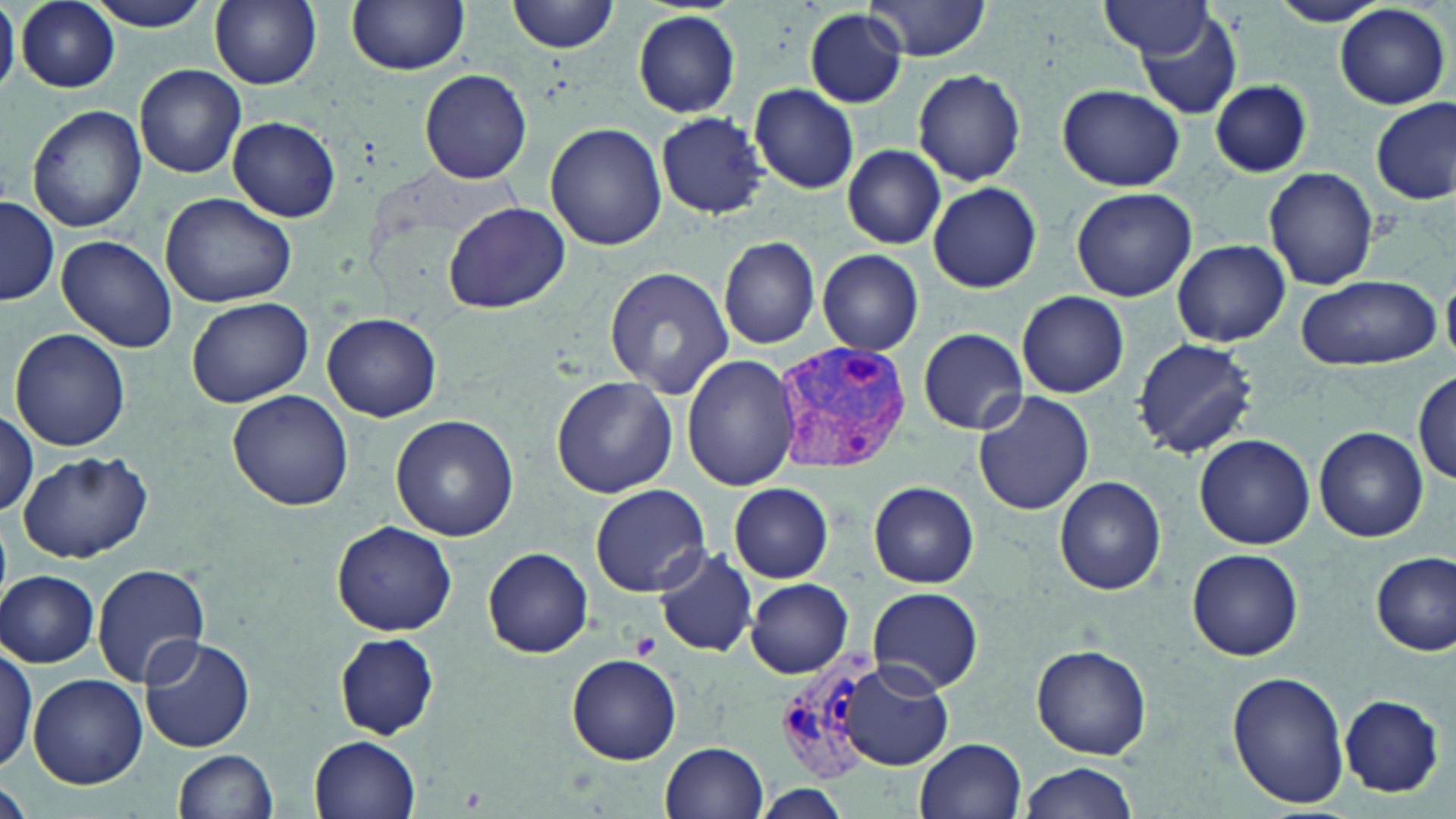

slide-level diagnosis = Plasmodium vivax
uninfected red blood cell locations = approximate bounding boxes as (x1, y1, x2, y2) in pixels: (86, 0, 217, 31), (208, 0, 322, 90), (508, 0, 619, 53), (862, 0, 993, 60), (1266, 0, 1389, 26), (346, 1, 470, 75), (15, 2, 120, 91), (1098, 2, 1213, 61), (0, 3, 19, 97), (1335, 5, 1449, 108), (805, 9, 906, 107), (1137, 9, 1242, 121), (632, 11, 740, 118), (135, 64, 246, 179), (417, 68, 533, 185), (913, 69, 1026, 185), (1209, 79, 1312, 177), (750, 84, 860, 195), (1057, 84, 1185, 191), (1372, 98, 1454, 205), (26, 104, 147, 232), (656, 110, 769, 219), (228, 117, 340, 221), (546, 122, 667, 249), (843, 145, 945, 249), (1263, 166, 1378, 291), (927, 182, 1042, 294), (1070, 187, 1198, 302), (160, 193, 300, 310), (1, 197, 60, 306), (443, 201, 570, 312), (56, 235, 178, 353), (718, 235, 822, 350), (1173, 239, 1290, 346), (817, 251, 925, 355), (605, 266, 732, 398), (1296, 273, 1442, 372), (1016, 291, 1129, 398), (187, 296, 314, 407), (323, 315, 442, 421), (9, 327, 131, 450), (918, 328, 1028, 436), (1132, 337, 1259, 460), (681, 354, 802, 490), (1413, 370, 1455, 487), (551, 375, 677, 498), (972, 389, 1093, 515), (227, 390, 354, 511), (0, 410, 39, 518), (390, 414, 519, 541), (1315, 427, 1427, 541), (1193, 433, 1316, 549), (17, 450, 152, 564), (1054, 476, 1167, 595), (868, 480, 979, 586), (728, 482, 833, 583), (590, 484, 709, 596), (332, 520, 458, 637), (483, 547, 593, 657), (654, 548, 757, 657), (1187, 548, 1304, 661), (1371, 551, 1455, 655), (91, 564, 210, 688), (2, 569, 100, 667), (745, 578, 854, 678), (866, 586, 982, 693), (335, 634, 438, 740), (136, 636, 254, 754), (1, 640, 37, 778), (1032, 644, 1153, 758), (567, 655, 683, 765), (842, 659, 955, 770), (1227, 672, 1348, 809), (27, 674, 147, 789), (1339, 693, 1446, 796), (310, 736, 420, 819), (917, 737, 1028, 819), (663, 740, 767, 817), (174, 749, 279, 819), (1021, 762, 1137, 818), (2, 773, 29, 819), (756, 784, 853, 819)
preparation = thin blood film
modality = light microscopy
stain = May-Grünwald-Giemsa
image size = 1456×819 pixels
Plasmodium vivax-infected red blood cell locations = approximate bounding boxes as (x1, y1, x2, y2) in pixels: (768, 339, 916, 473), (777, 647, 880, 782)
platelet locations = approximate bounding boxes as (x1, y1, x2, y2) in pixels: (629, 633, 661, 660)
field of view = single
magnification = 1000x